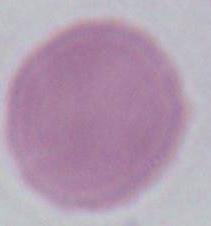
Summary:
  - Magnification: 1000x
  - Modality: micrograph
  - Identification: erythrocyte